Identify the parasite.
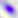
This is Toxoplasma gondii.

Summary:
  - Magnification: 400x
  - Modality: micrograph